Name the parasite shown.
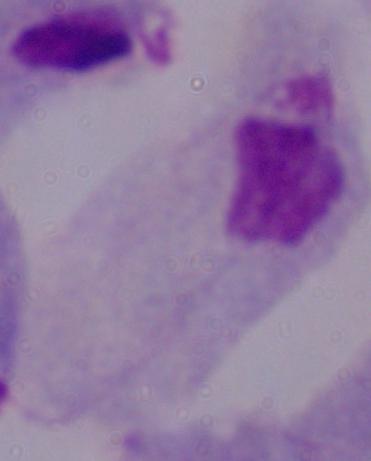
This is a trichomonad.

Summary:
  - Magnification: 1000x
  - Modality: photomicrograph